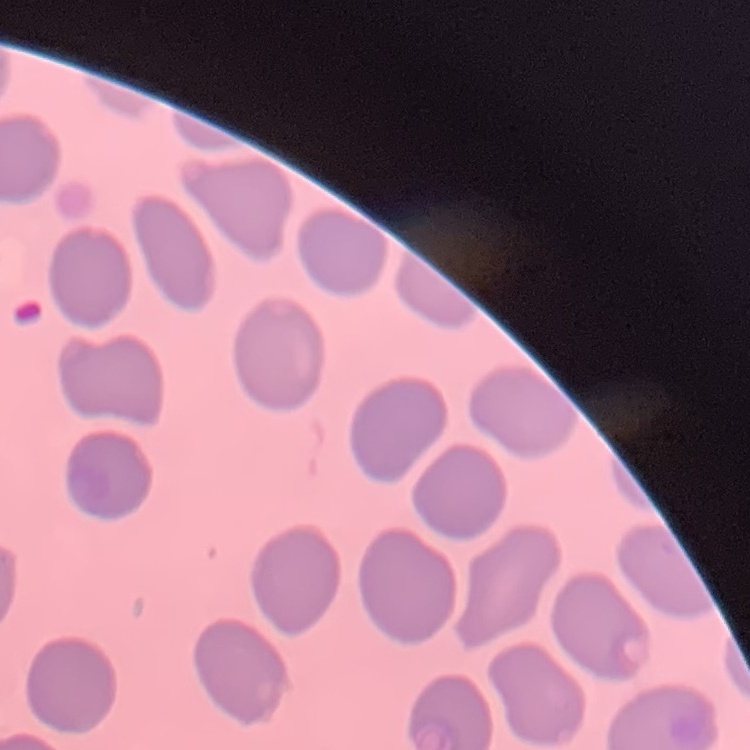
red blood cell morphology = no rouleaux formation
image type = square crop of a larger photomicrograph
stain = Field's or Giemsa
preparation = thin blood smear